Point out each Plasmodium parasite.
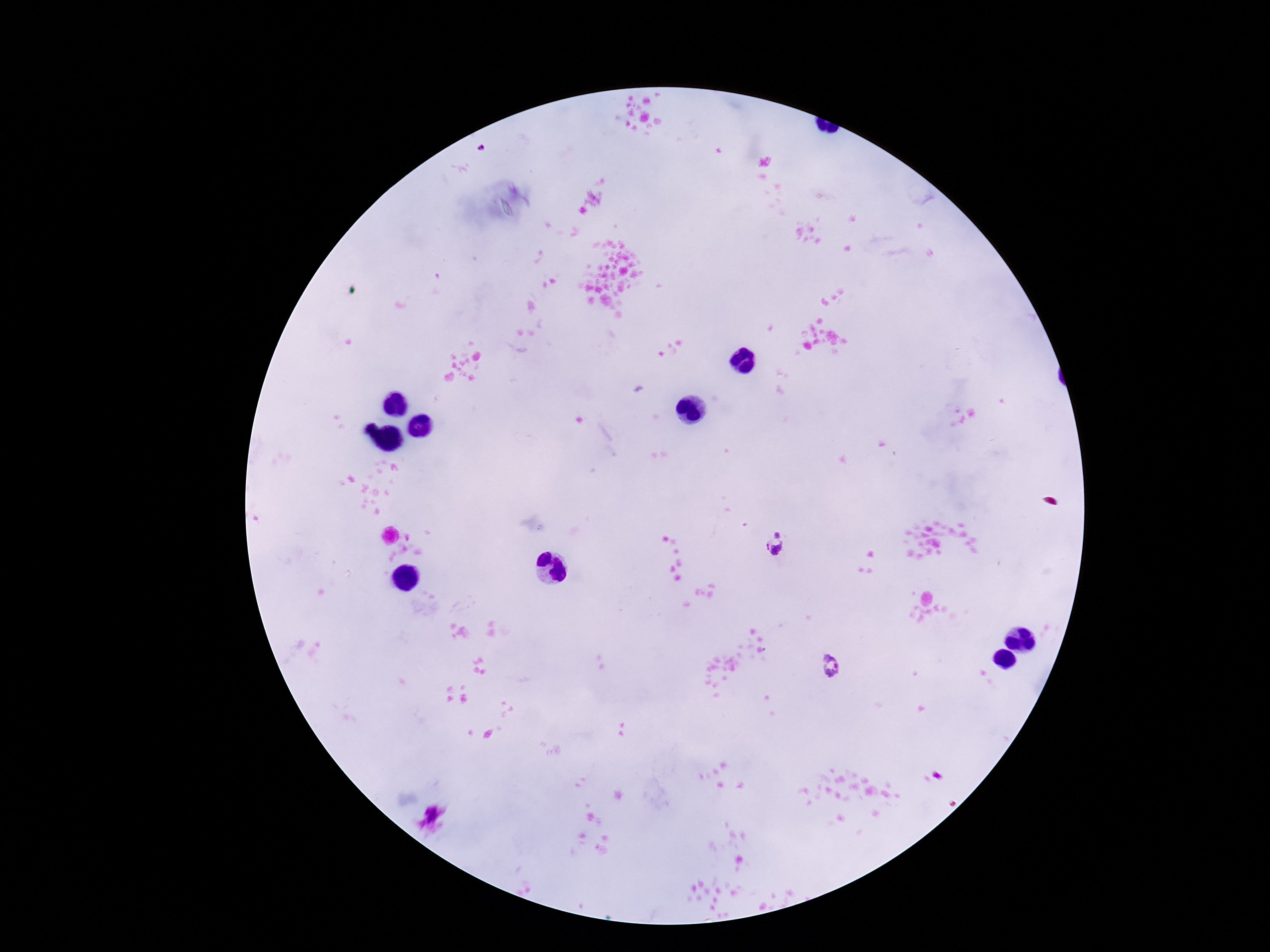

Approximate object centers, in pixels from the top-left corner.
Plasmodium parasites: (x=778, y=533), (x=774, y=549), (x=832, y=666).

Summary:
  - Stain: Giemsa
  - Preparation: thick peripheral-blood smear
  - Image size: 1270×952 pixels
  - Magnification: 100x
  - Field of view: one from this slide
  - Patient malaria status: positive
  - Capture: smartphone camera through the microscope eyepiece